Classify this cell by malaria status.
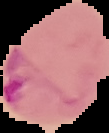

Parasitized.

Image is 109×133 pixels. The area outside the segmented cell region is set to black. From a thin blood smear.